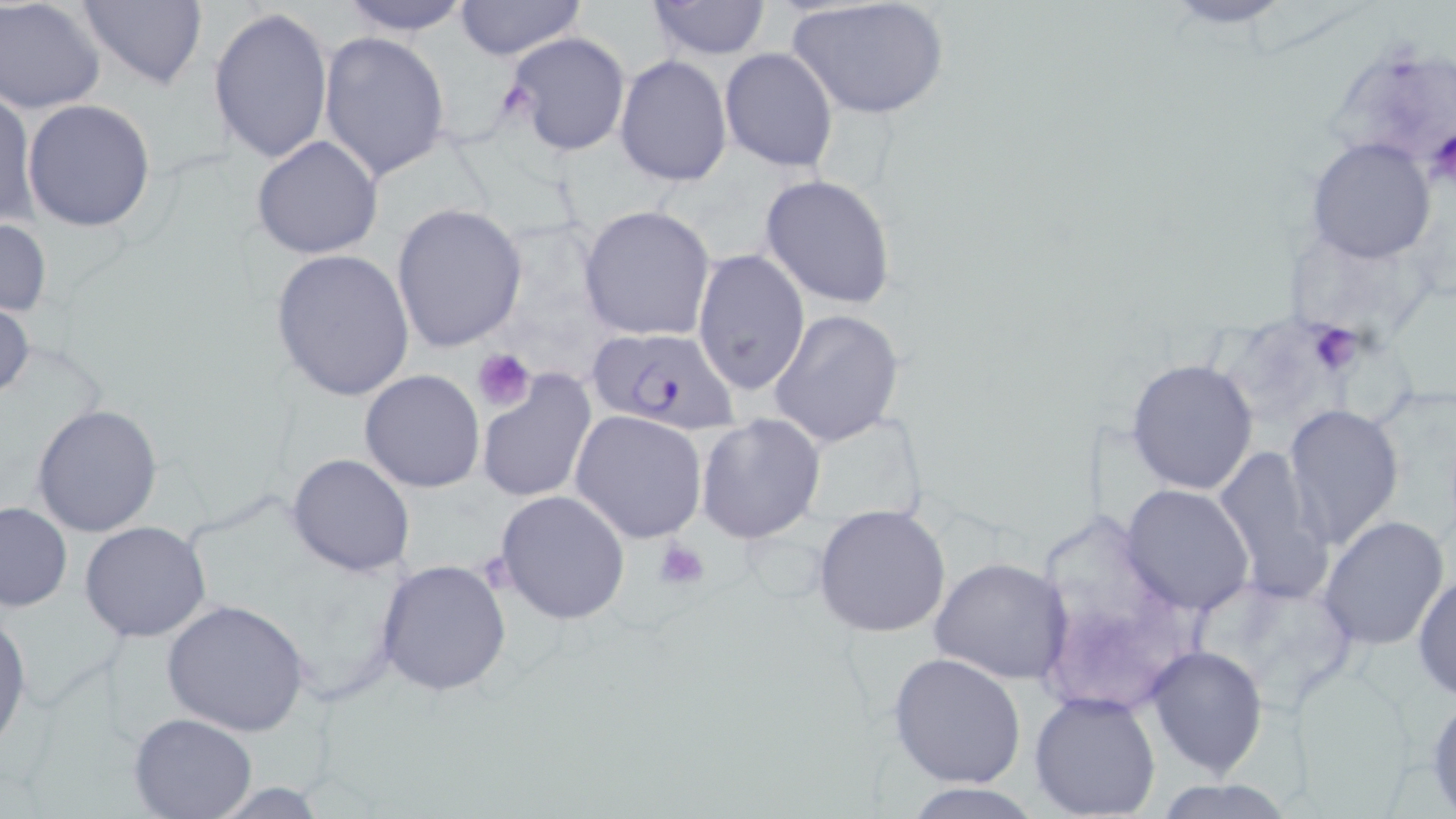 Approximate bounding boxes as (x1, y1, x2, y2) in pixels. Platelet locations: (1424, 124, 1456, 185), (1298, 324, 1370, 378), (471, 350, 535, 414), (655, 538, 711, 591). Plasmodium falciparum-infected red blood cell locations: (587, 327, 741, 435). Uninfected red blood cell locations: (1, 0, 106, 114), (75, 0, 206, 91), (335, 0, 475, 37), (646, 0, 772, 59), (1156, 0, 1303, 30), (454, 1, 585, 62), (786, 1, 949, 121), (208, 5, 333, 165), (318, 31, 451, 183), (507, 31, 632, 158), (719, 48, 838, 173), (615, 55, 732, 186), (0, 93, 36, 228), (23, 99, 156, 232), (250, 134, 383, 260), (1307, 138, 1436, 263), (760, 174, 896, 308), (391, 203, 527, 351), (578, 205, 715, 342), (0, 216, 52, 321), (272, 248, 413, 402), (692, 249, 811, 397), (0, 294, 34, 406), (767, 309, 905, 448), (1124, 357, 1260, 494), (358, 369, 486, 493), (476, 375, 595, 504), (31, 403, 163, 537), (1282, 404, 1403, 551), (571, 410, 709, 542), (695, 412, 824, 543), (1210, 448, 1335, 601), (287, 453, 415, 577), (1120, 484, 1256, 616), (494, 490, 630, 624), (0, 503, 70, 613), (812, 503, 951, 636), (1021, 507, 1213, 728), (1318, 514, 1450, 652), (80, 521, 212, 643), (374, 557, 514, 696), (929, 557, 1072, 684), (1414, 569, 1455, 705), (162, 599, 310, 736), (0, 610, 30, 748), (1145, 644, 1270, 777), (889, 653, 1026, 790), (1029, 689, 1161, 819), (1426, 690, 1456, 814), (130, 711, 255, 817), (1154, 778, 1295, 818), (901, 783, 1045, 818). Slide-level diagnosis: Plasmodium falciparum. Thin blood smear. Optical microscopy. Captured at 1000x magnification. Single field of view. May-Grünwald-Giemsa stain. Image is 1456×819 pixels.